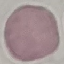

malaria_status: uninfected
capture: smartphone camera at the microscope eyepiece
preparation: thin blood smear
stain: Giemsa
image_type: automatically extracted cell patch, resized to 64 × 64 pixels